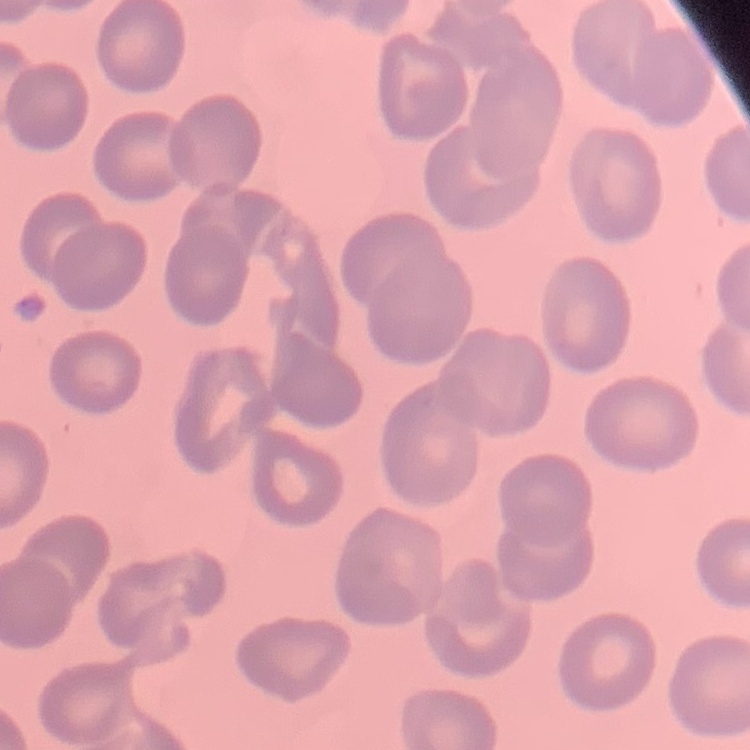
The erythrocytes exhibit no rouleaux formation. Square crop of a larger photomicrograph. Stained with either Field's or Giemsa. Thin blood smear.